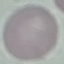
malaria status = uninfected
image type = automatically extracted cell patch, resized to 64 × 64 pixels
stain = Giemsa
preparation = thin smear
capture = smartphone camera at the microscope eyepiece